Locate and identify every blood parasite.
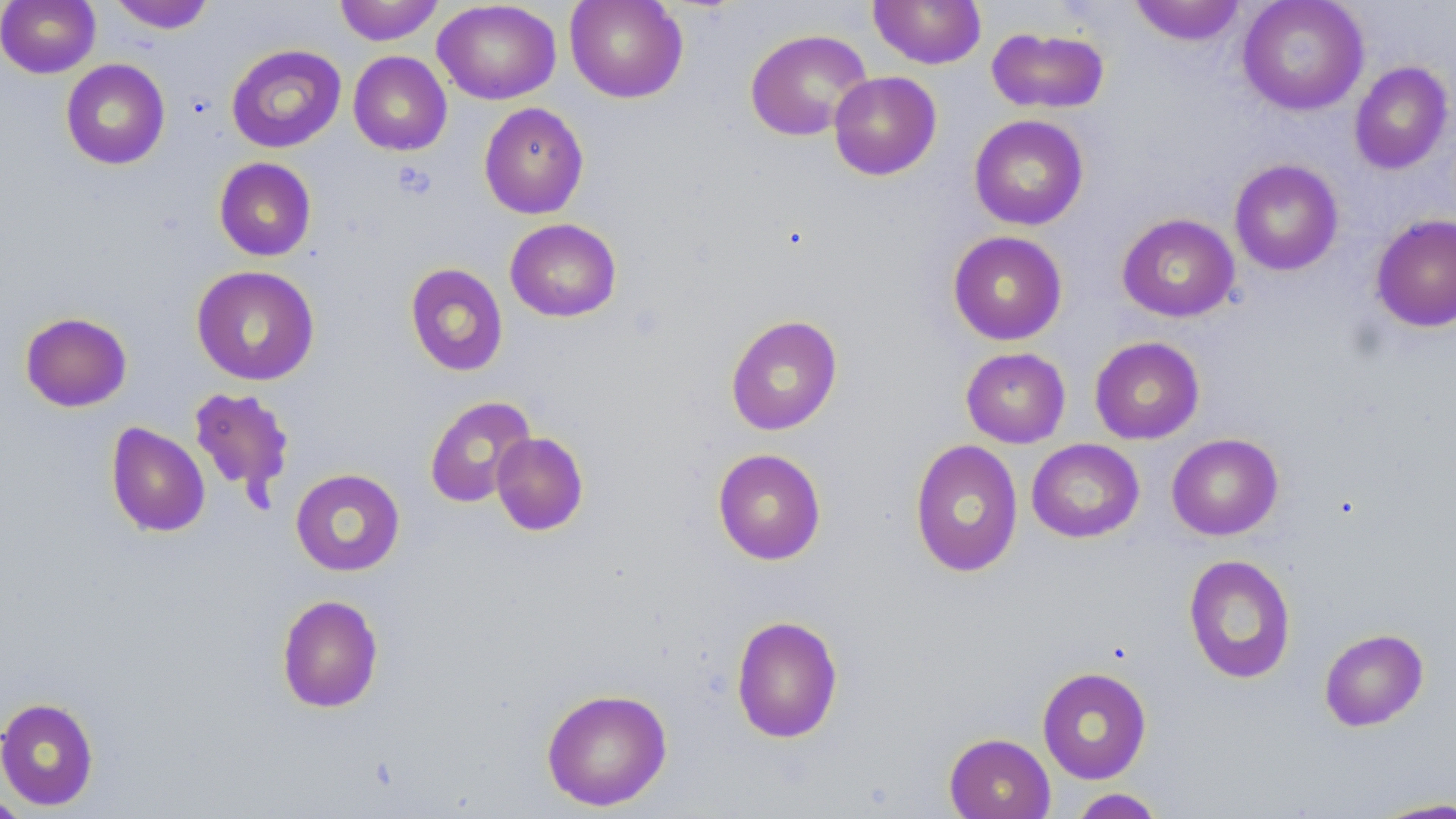
No blood parasites observed.

Approximate bounding boxes as (x1,y1)-(x2,y2) corner pairs in pixels. Platelet locations: (394,160)-(437,201). Uninfected red blood cell locations: (1,0)-(101,78), (334,0)-(444,45), (564,0)-(688,103), (869,0)-(986,69), (1237,0)-(1369,116), (108,1)-(216,34), (433,1)-(561,105), (1129,1)-(1247,46), (987,27)-(1110,114), (744,28)-(872,141), (226,44)-(346,153), (348,51)-(452,156), (60,58)-(170,170), (1349,62)-(1453,174), (828,71)-(942,180), (478,102)-(589,219), (969,114)-(1089,231), (214,157)-(317,261), (1229,159)-(1344,275), (1117,213)-(1240,323), (1370,214)-(1456,333), (505,218)-(622,322), (947,230)-(1068,345), (405,263)-(508,377), (191,265)-(320,386), (19,311)-(133,413), (725,314)-(843,436), (1089,336)-(1204,444), (961,347)-(1071,448), (187,386)-(295,506), (423,395)-(536,509), (105,422)-(211,537), (491,431)-(589,536), (1167,433)-(1283,540), (909,439)-(1024,578), (1027,439)-(1144,543), (712,448)-(826,565), (290,468)-(405,577), (1183,554)-(1297,684), (277,594)-(384,713), (730,614)-(843,744), (1318,628)-(1429,731), (1037,666)-(1152,784), (540,687)-(673,812), (0,697)-(100,811), (944,733)-(1055,819), (1067,788)-(1166,819), (0,792)-(31,818), (1365,797)-(1456,818). Slide-level diagnosis: no evidence of blood parasites. One field of a larger specimen. Light microscopy. Thin blood smear. Image is 1456×819 pixels. May-Grünwald-Giemsa stain. Captured at 1000x magnification.